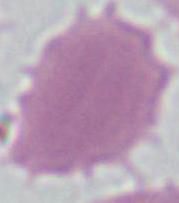
Summary:
  - Magnification: 1000x
  - Identification: red blood cell
  - Modality: micrograph